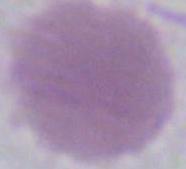

modality = micrograph
magnification = 1000x
identification = red blood cell